Identify the preparation type.
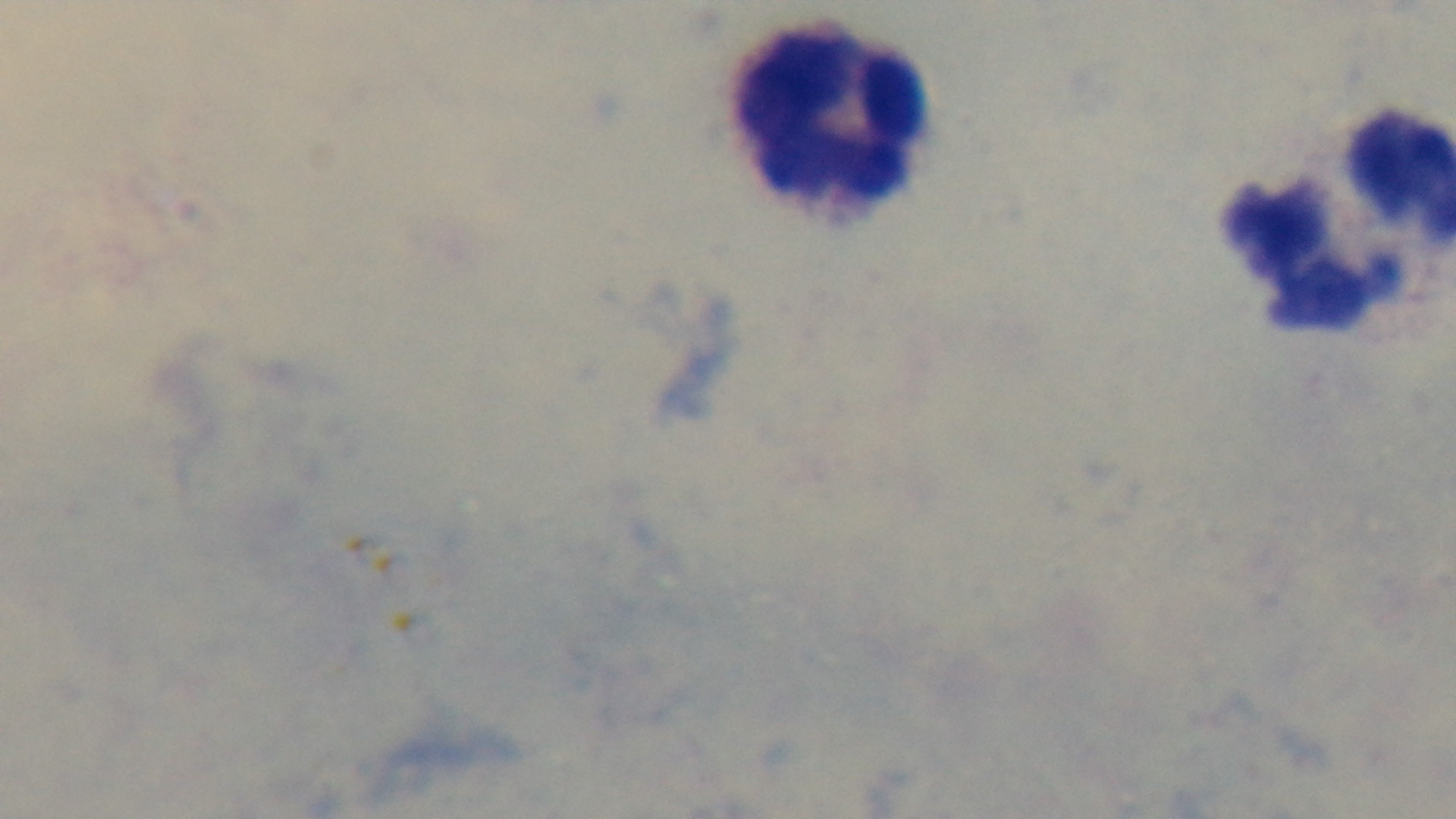

It is a thick blood film.

malaria_status: uninfected
field_of_view: single
modality: light microscopy
capture: mounted 4K digital camera
objective: 100x oil immersion
stain: Giemsa